Evaluate for malaria.
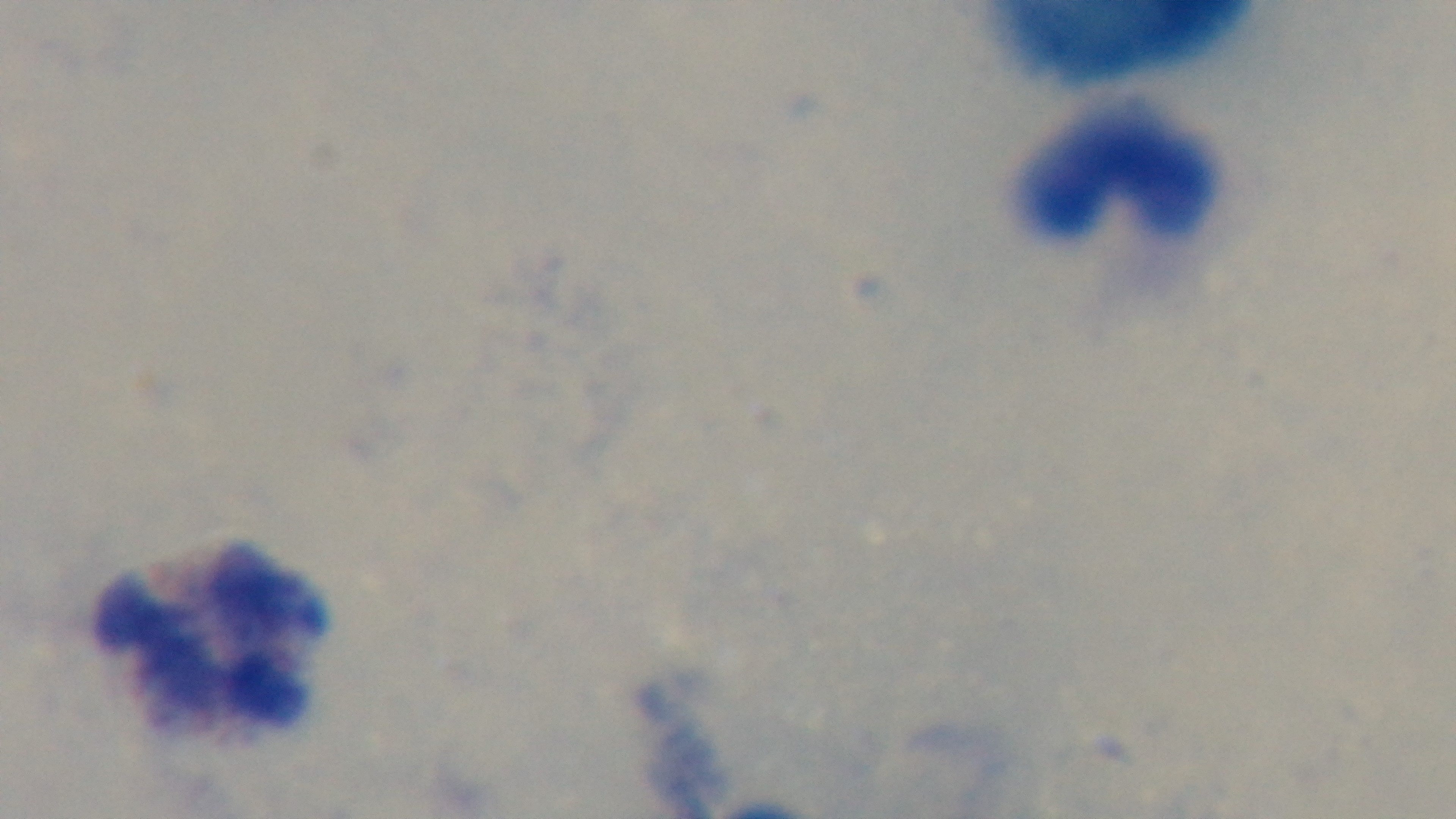
Uninfected.

Mounted 4K digital camera. One field from the slide. Oil-immersion objective, 100x. Giemsa-stained. Preparation: thick. Light microscopy.